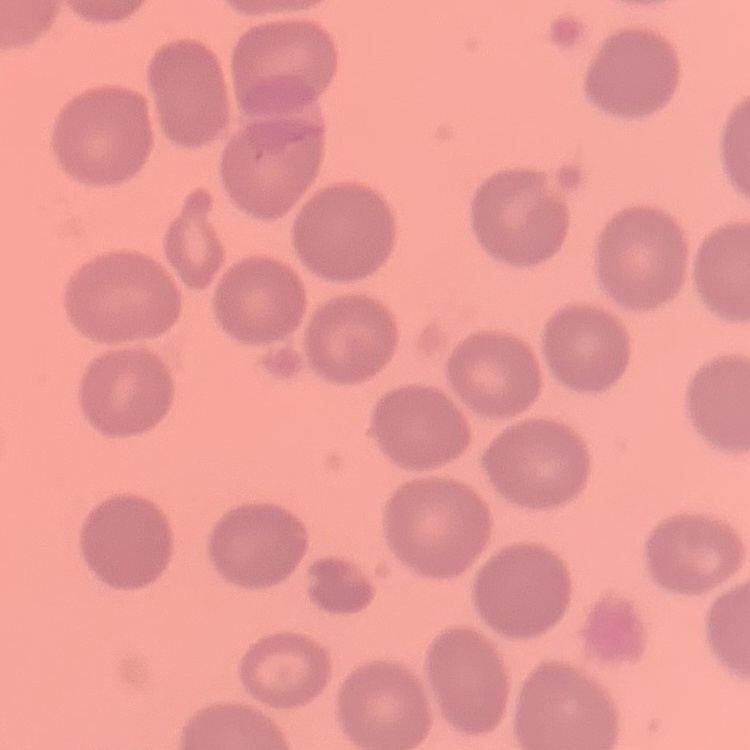

erythrocyte_morphology: no rouleaux formation
preparation: thin blood film
image_type: one tile cut from a larger photomicrograph
stain: Field's or Giemsa